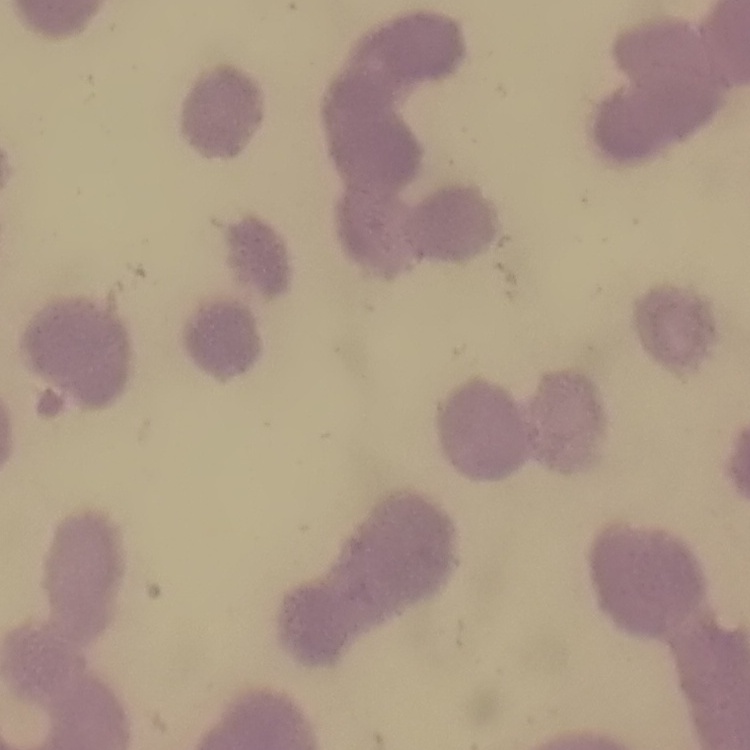 The red blood cells exhibit rouleaux formation. Field's or Giemsa stain. One tile cut from a larger photomicrograph. Thin blood smear.